Outline each blood parasite and name the species.
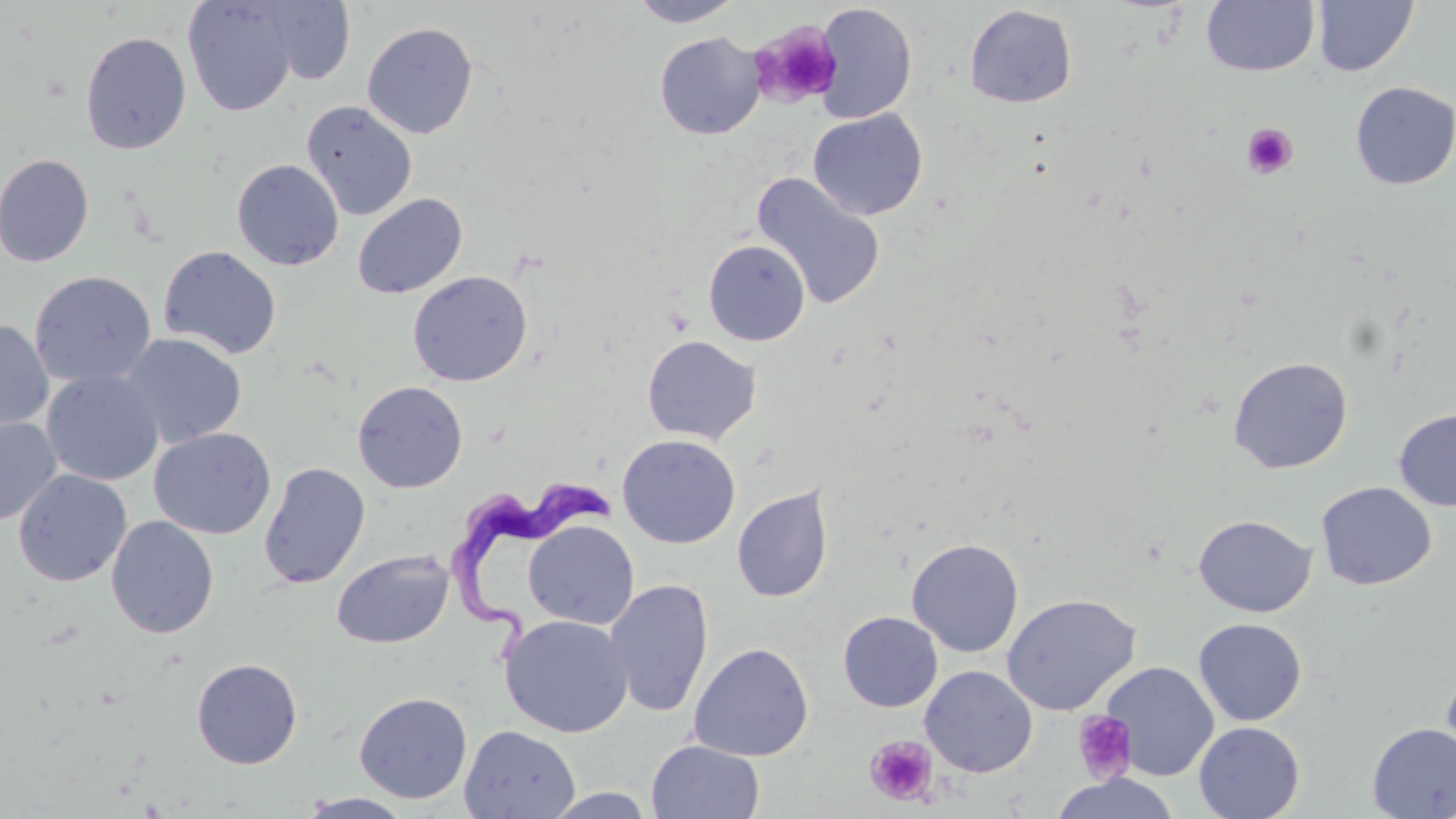
Approximate bounding boxes as (x1,y1)-(x2,y2) corner pairs in pixels.
Trypanosoma brucei: (445,479)-(614,679).
No Plasmodium falciparum, Plasmodium ovale, Plasmodium malariae, Plasmodium vivax, or Babesia divergens observed.

Summary:
  - Platelet locations: (747,20)-(842,109), (1241,123)-(1299,179), (1072,711)-(1137,784), (865,735)-(938,806)
  - Uninfected red blood cell locations: (627,0)-(745,27), (1313,0)-(1418,77), (182,1)-(298,117), (257,1)-(356,84), (1201,1)-(1319,77), (813,3)-(917,124), (964,4)-(1078,109), (361,21)-(479,139), (79,31)-(191,155), (654,32)-(765,140), (1350,80)-(1456,190), (301,101)-(417,221), (808,109)-(928,220), (0,153)-(94,267), (231,159)-(344,271), (750,172)-(887,310), (352,193)-(467,299), (703,239)-(811,346), (158,245)-(282,359), (407,270)-(532,387), (29,271)-(156,389), (0,318)-(54,432), (119,333)-(247,448), (642,335)-(762,445), (1228,356)-(1353,473), (42,370)-(164,486), (352,380)-(468,493), (1394,407)-(1456,511), (0,417)-(62,525), (149,427)-(276,539), (617,434)-(741,549), (258,461)-(370,589), (13,469)-(132,587), (1316,481)-(1436,591), (731,484)-(834,604), (1193,514)-(1316,617), (105,515)-(219,639), (523,520)-(639,630), (906,538)-(1024,657), (332,550)-(454,649), (604,578)-(714,718), (1001,593)-(1141,715), (838,611)-(943,712), (499,614)-(633,737), (1193,618)-(1307,726), (688,642)-(814,761), (191,658)-(303,769), (1441,658)-(1456,772), (1102,662)-(1219,781), (920,665)-(1038,777), (353,692)-(473,804), (1193,721)-(1305,819), (1367,723)-(1456,818), (460,725)-(580,819), (646,739)-(765,819), (1049,772)-(1181,819), (542,788)-(656,818), (298,792)-(415,818)
  - Slide-level diagnosis: Trypanosoma brucei
  - Image size: 1456×819 pixels
  - Stain: May-Grünwald-Giemsa
  - Modality: optical microscopy
  - Preparation: thin blood smear
  - Field of view: single
  - Magnification: 1000x